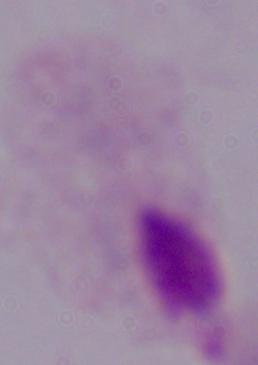
Photomicrograph. A trichomonad is shown. Captured at 1000x magnification.